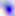
Toxoplasma gondii is seen. Micrograph. 400x magnification.